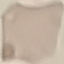

Result: no malaria parasites seen. Automatically extracted cell patch, resized to 64 × 64 pixels. Giemsa stain. Photographed with a smartphone camera at the microscope eyepiece. Thin blood smear.